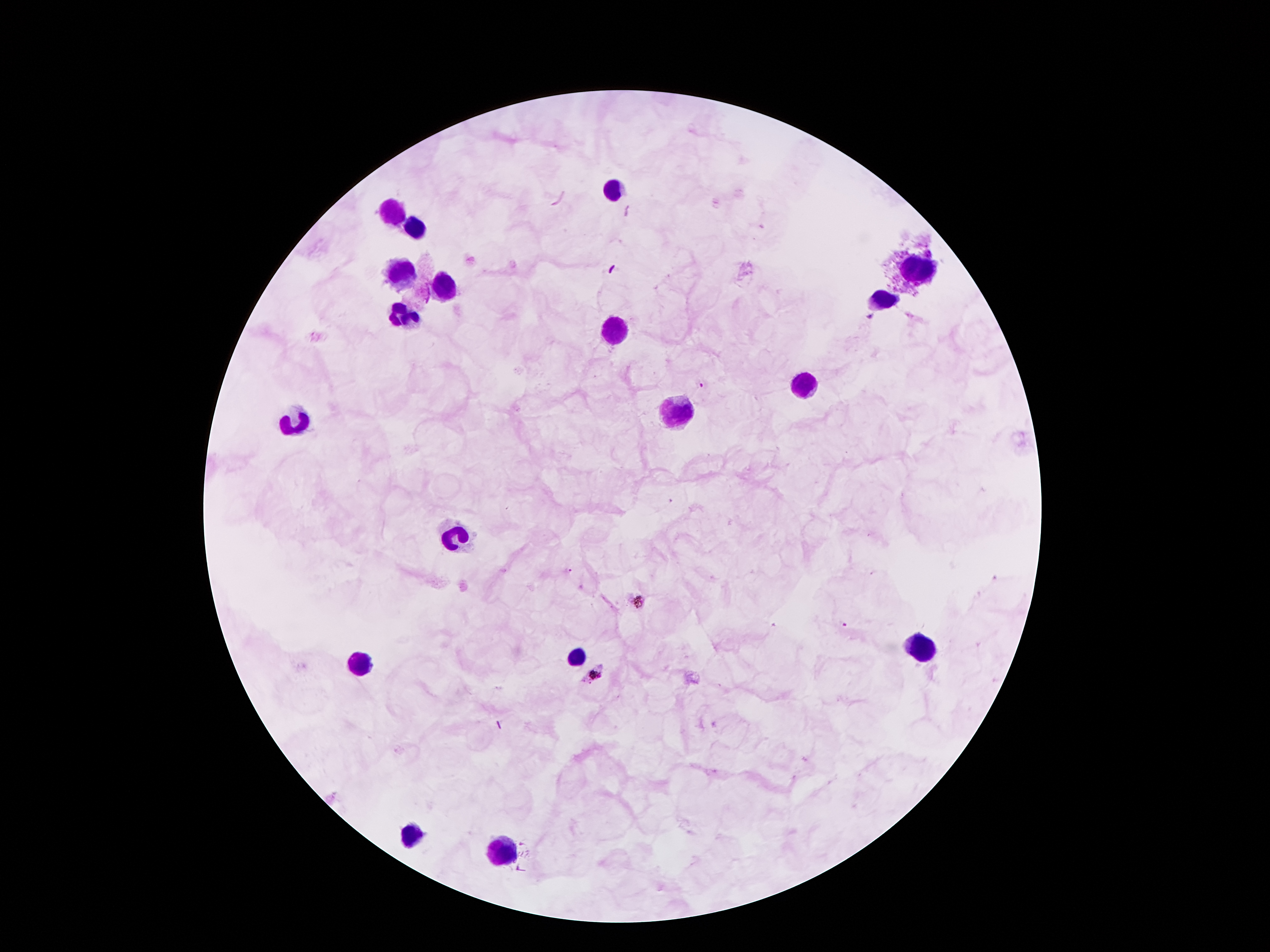
{
  "stain": "Giemsa",
  "magnification": "100x",
  "patient_malaria_status": "infected with Plasmodium falciparum",
  "plasmodium_parasite_locations": "approximate centers as (x, y) in pixels: (870, 317), (702, 385), (568, 571), (634, 599), (844, 624), (593, 675)",
  "preparation": "thick blood smear",
  "image_size": "1270×952 pixels",
  "capture": "smartphone camera through the microscope eyepiece",
  "field_of_view": "one from this slide",
  "leukocyte_locations": "approximate centers as (x, y) in pixels: (615, 188), (393, 211), (416, 228), (403, 269), (917, 269), (445, 286), (884, 299), (407, 314), (615, 330), (800, 385), (678, 410), (298, 421), (456, 538), (922, 646), (575, 658), (355, 664), (413, 835), (500, 849)"
}